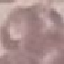

Summary:
  - Malaria status: uninfected
  - Stain: Giemsa
  - Preparation: thin blood smear
  - Image type: automatically extracted cell patch, resized to 64 × 64 pixels
  - Capture: smartphone through the microscope eyepiece